Name the blood parasite species.
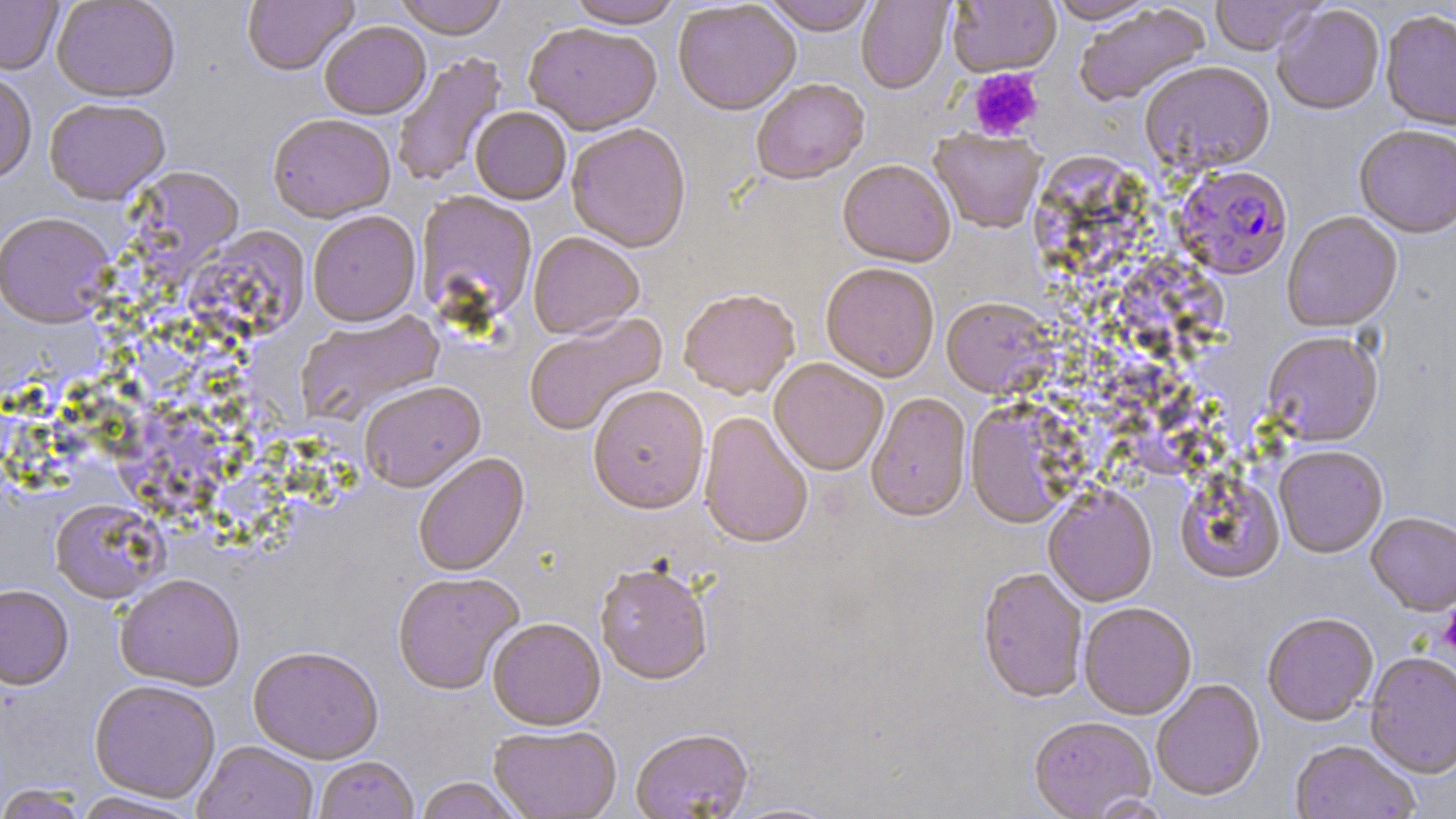
Plasmodium falciparum.

Summary:
  - Coordinate format: approximate bounding boxes as named x1/y1/x2/y2 corners in pixels
  - Platelet locations: (x1=967, y1=68, x2=1043, y2=141), (x1=1437, y1=606, x2=1456, y2=658)
  - Plasmodium falciparum-infected red blood cell locations: (x1=1173, y1=164, x2=1293, y2=280)
  - Uninfected red blood cell locations: (x1=0, y1=0, x2=63, y2=75), (x1=51, y1=0, x2=180, y2=102), (x1=242, y1=0, x2=358, y2=76), (x1=393, y1=0, x2=509, y2=40), (x1=565, y1=0, x2=684, y2=29), (x1=760, y1=0, x2=878, y2=36), (x1=1046, y1=0, x2=1158, y2=24), (x1=1210, y1=0, x2=1322, y2=56), (x1=856, y1=1, x2=953, y2=94), (x1=948, y1=1, x2=1061, y2=77), (x1=673, y1=2, x2=801, y2=116), (x1=1074, y1=4, x2=1212, y2=108), (x1=1272, y1=4, x2=1385, y2=116), (x1=1380, y1=10, x2=1456, y2=132), (x1=319, y1=21, x2=431, y2=120), (x1=524, y1=23, x2=662, y2=136), (x1=392, y1=52, x2=508, y2=190), (x1=1139, y1=61, x2=1275, y2=177), (x1=0, y1=70, x2=37, y2=183), (x1=751, y1=80, x2=870, y2=187), (x1=44, y1=98, x2=170, y2=204), (x1=470, y1=107, x2=571, y2=206), (x1=267, y1=115, x2=396, y2=223), (x1=566, y1=124, x2=691, y2=254), (x1=1354, y1=125, x2=1456, y2=238), (x1=930, y1=130, x2=1046, y2=234), (x1=838, y1=161, x2=955, y2=269), (x1=124, y1=166, x2=245, y2=275), (x1=415, y1=192, x2=538, y2=326), (x1=0, y1=212, x2=116, y2=327), (x1=308, y1=212, x2=421, y2=327), (x1=1282, y1=212, x2=1403, y2=333), (x1=183, y1=225, x2=310, y2=348), (x1=528, y1=232, x2=644, y2=340), (x1=820, y1=265, x2=939, y2=383), (x1=679, y1=292, x2=800, y2=401), (x1=941, y1=298, x2=1055, y2=401), (x1=297, y1=310, x2=447, y2=428), (x1=524, y1=315, x2=667, y2=437), (x1=1262, y1=332, x2=1383, y2=447), (x1=769, y1=360, x2=888, y2=478), (x1=359, y1=381, x2=486, y2=494), (x1=588, y1=386, x2=710, y2=516), (x1=865, y1=394, x2=971, y2=524), (x1=965, y1=402, x2=1075, y2=530), (x1=698, y1=412, x2=813, y2=550), (x1=1274, y1=445, x2=1387, y2=558), (x1=414, y1=453, x2=529, y2=577), (x1=1174, y1=470, x2=1285, y2=585), (x1=1043, y1=488, x2=1157, y2=607), (x1=50, y1=498, x2=166, y2=603), (x1=1365, y1=513, x2=1456, y2=615), (x1=595, y1=566, x2=712, y2=687), (x1=976, y1=570, x2=1088, y2=705), (x1=392, y1=572, x2=524, y2=695), (x1=115, y1=574, x2=245, y2=690), (x1=0, y1=584, x2=73, y2=689), (x1=1079, y1=604, x2=1197, y2=721), (x1=1262, y1=614, x2=1378, y2=728), (x1=488, y1=620, x2=605, y2=732), (x1=248, y1=647, x2=384, y2=764), (x1=1364, y1=653, x2=1456, y2=779), (x1=89, y1=680, x2=221, y2=803), (x1=1151, y1=680, x2=1265, y2=803), (x1=1029, y1=718, x2=1155, y2=818), (x1=488, y1=727, x2=622, y2=819), (x1=631, y1=731, x2=752, y2=818), (x1=1289, y1=741, x2=1419, y2=819), (x1=193, y1=742, x2=318, y2=819), (x1=314, y1=757, x2=419, y2=819), (x1=413, y1=778, x2=525, y2=819), (x1=0, y1=784, x2=91, y2=819), (x1=70, y1=792, x2=205, y2=818), (x1=724, y1=800, x2=847, y2=819)
  - Modality: light microscopy
  - Image size: 1456×819 pixels
  - Stain: May-Grünwald-Giemsa
  - Field of view: one of a larger specimen
  - Preparation: thin blood film
  - Magnification: 1000x